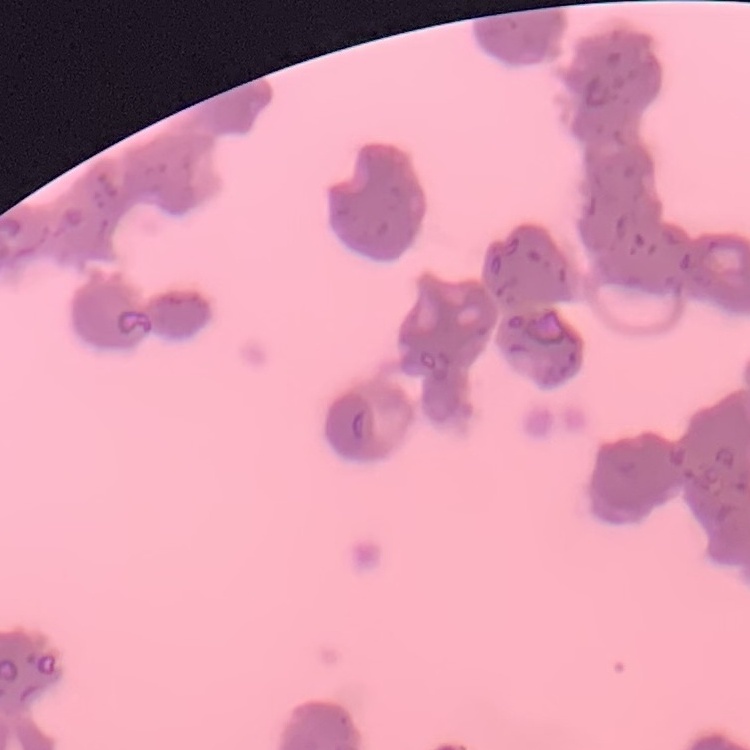
The erythrocytes show rouleaux formation. Field's or Giemsa stain. Thin blood film. One tile cut from a larger photomicrograph.